Outline every parasitised red blood cell, every trophozoite, every gametocyte, every leukocyte, and every artifact (platelet-like body, stain precipitate, or debris).
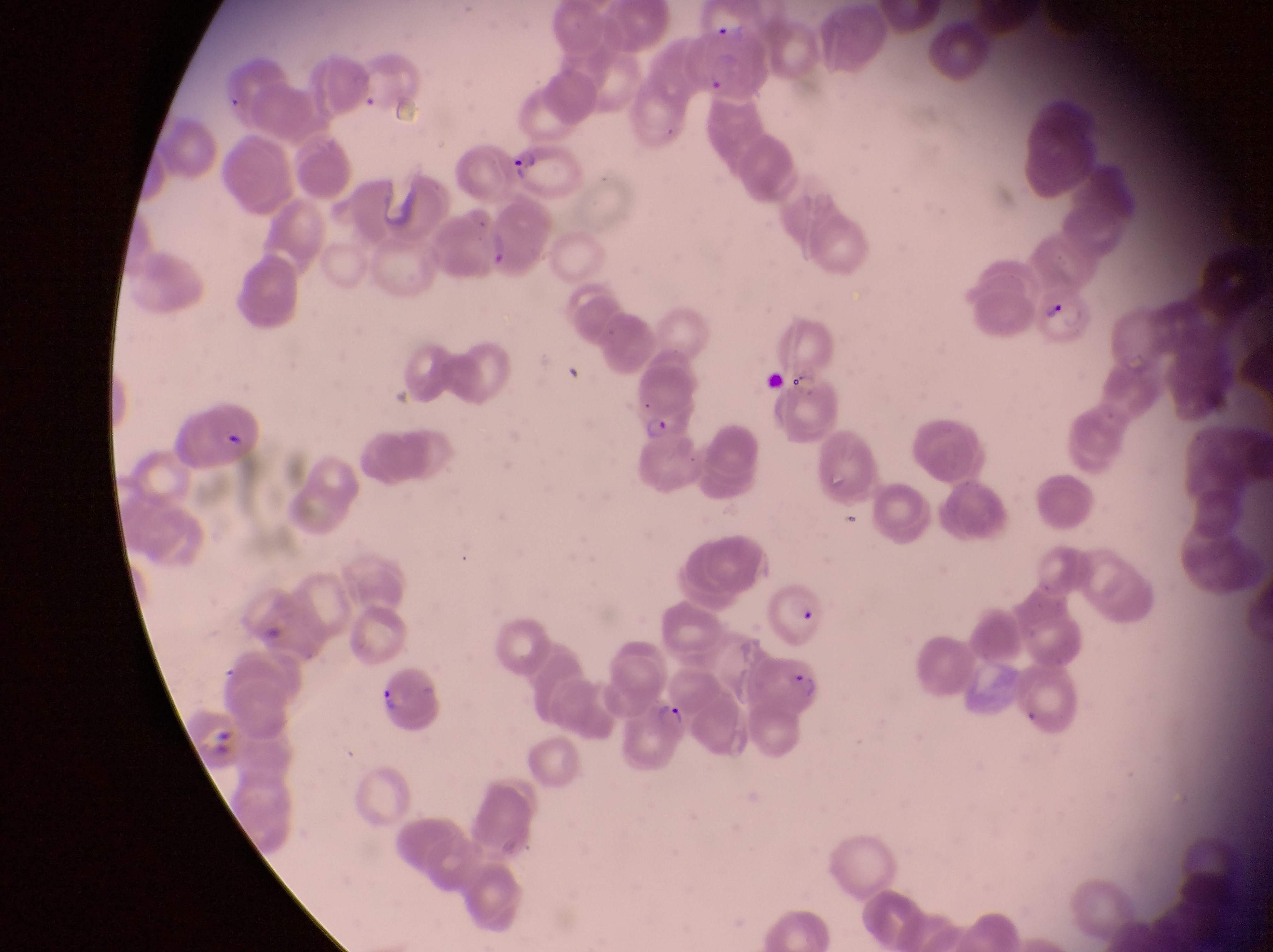
Approximate bounding boxes as left top right bottom in pixels.
Parasitised red blood cells: 684 33 769 96; 507 137 585 202; 769 579 827 649; 749 642 824 717; 378 669 438 727.
Trophozoites: 1044 294 1069 326; 644 409 676 449; 652 697 689 734.
No leukocytes observed.

field of view = single
magnification = 1000x
capture = smartphone photograph through the eyepiece of an Olympus CX-23 microscope
preparation = thin blood smear
country = Uganda
image size = 1273×952 pixels